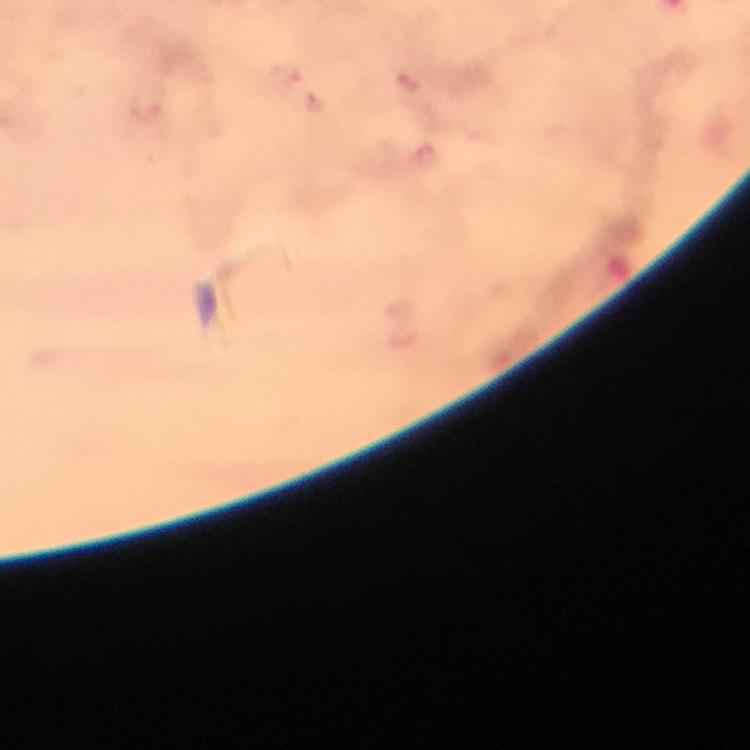
Approximate centers as (x, y) in pixels.
Summary:
  - Plasmodium parasite locations: (283, 77), (409, 85), (316, 104), (428, 158)
  - Preparation: thick blood smear
  - Capture: smartphone photograph through a microscope
  - Image size: 750×750 pixels
  - Stain: Giemsa
  - Context: from a malaria diagnostic workup
  - Cropped from: a single field of view
  - Immersion oil: applied
  - Magnification: 100x